Assess this cell for malaria.
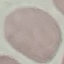

Uninfected.

Cell patch, automatically extracted from a larger field of view and resized to 64 × 64 pixels. Acquired by smartphone through the microscope eyepiece. Giemsa-stained preparation. Thin blood smear.